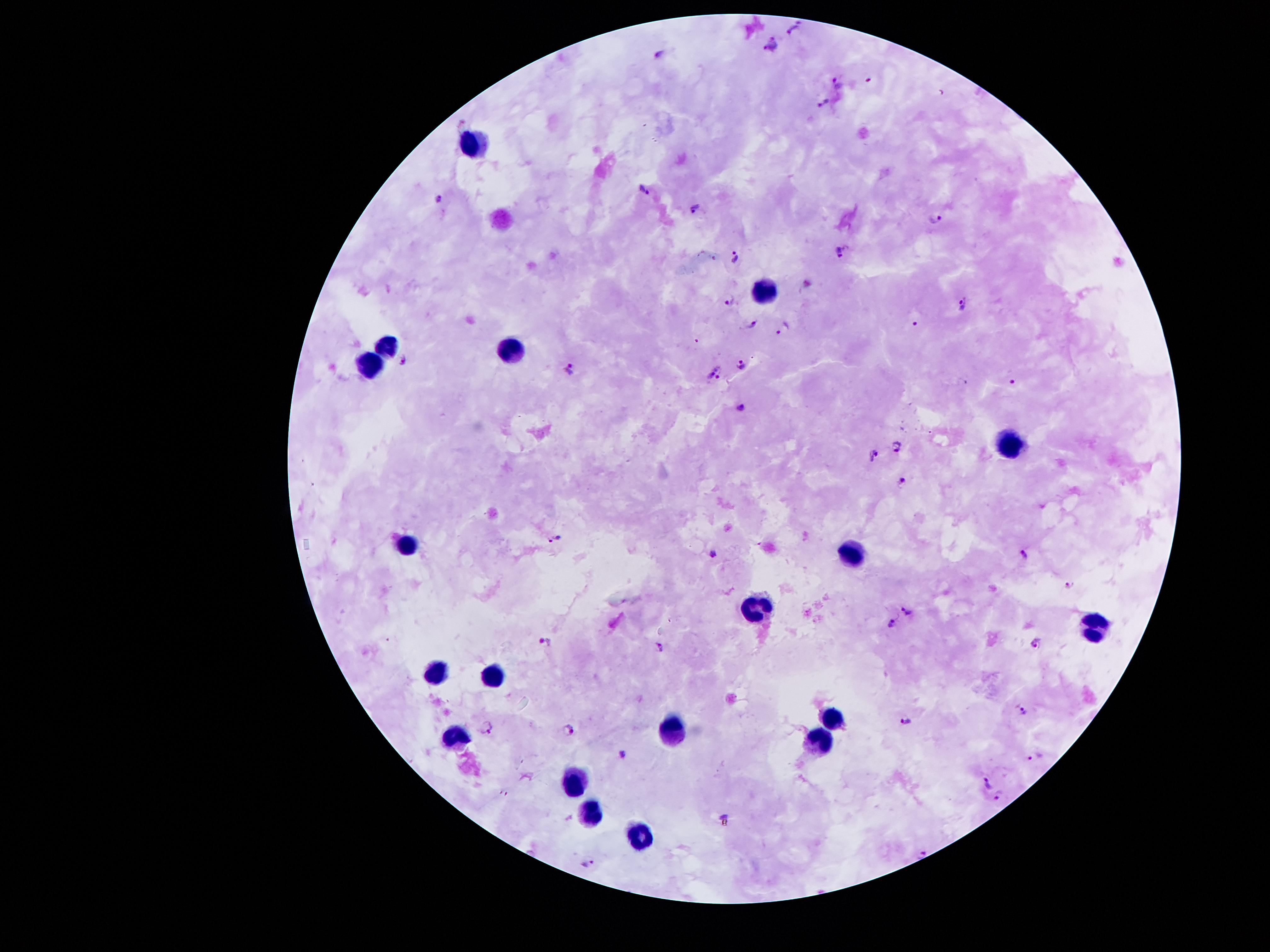 Approximate centers as (x, y) in pixels. Leukocyte locations: (471, 138), (768, 287), (389, 341), (517, 353), (375, 364), (1009, 446), (408, 542), (846, 551), (754, 603), (1093, 626), (435, 671), (493, 673), (835, 713), (668, 729), (454, 737), (818, 742), (573, 779), (586, 810), (639, 838). Plasmodium parasite locations: (794, 30), (771, 45), (661, 54), (838, 82), (822, 104), (645, 190), (438, 197), (697, 209), (936, 218), (841, 253), (736, 257), (729, 299), (962, 303), (751, 322), (914, 323), (781, 328), (402, 359), (741, 364), (571, 367), (715, 373), (1012, 381), (741, 405), (895, 447), (874, 455), (903, 479), (556, 540), (713, 551), (1024, 556), (1069, 583), (906, 611), (891, 621), (545, 644), (1034, 644), (659, 645), (1022, 709), (905, 719), (484, 728), (570, 729), (623, 755), (1036, 756), (986, 782), (504, 793), (1000, 795), (725, 821), (924, 852), (589, 863). Image is 1270×952 pixels. 100x magnification. Photographed through the microscope eyepiece with a smartphone camera. One field from this slide. Giemsa stain. Patient malaria status: positive for Plasmodium falciparum. Thick blood film.